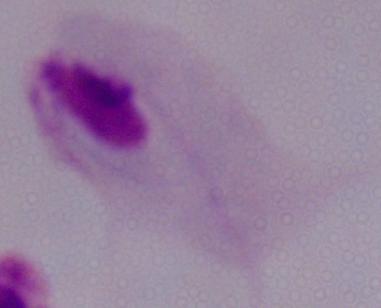

modality = photomicrograph
magnification = 1000x
identification = trichomonad